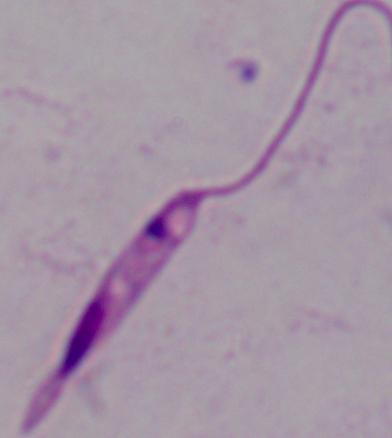
Summary:
  - Identification: Leishmania
  - Modality: photomicrograph
  - Magnification: 1000x